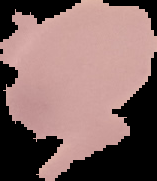
Summary:
  - Malaria status: uninfected
  - Image type: segmented cell region on a black background
  - Image size: 157×181 pixels
  - Preparation: thin blood smear